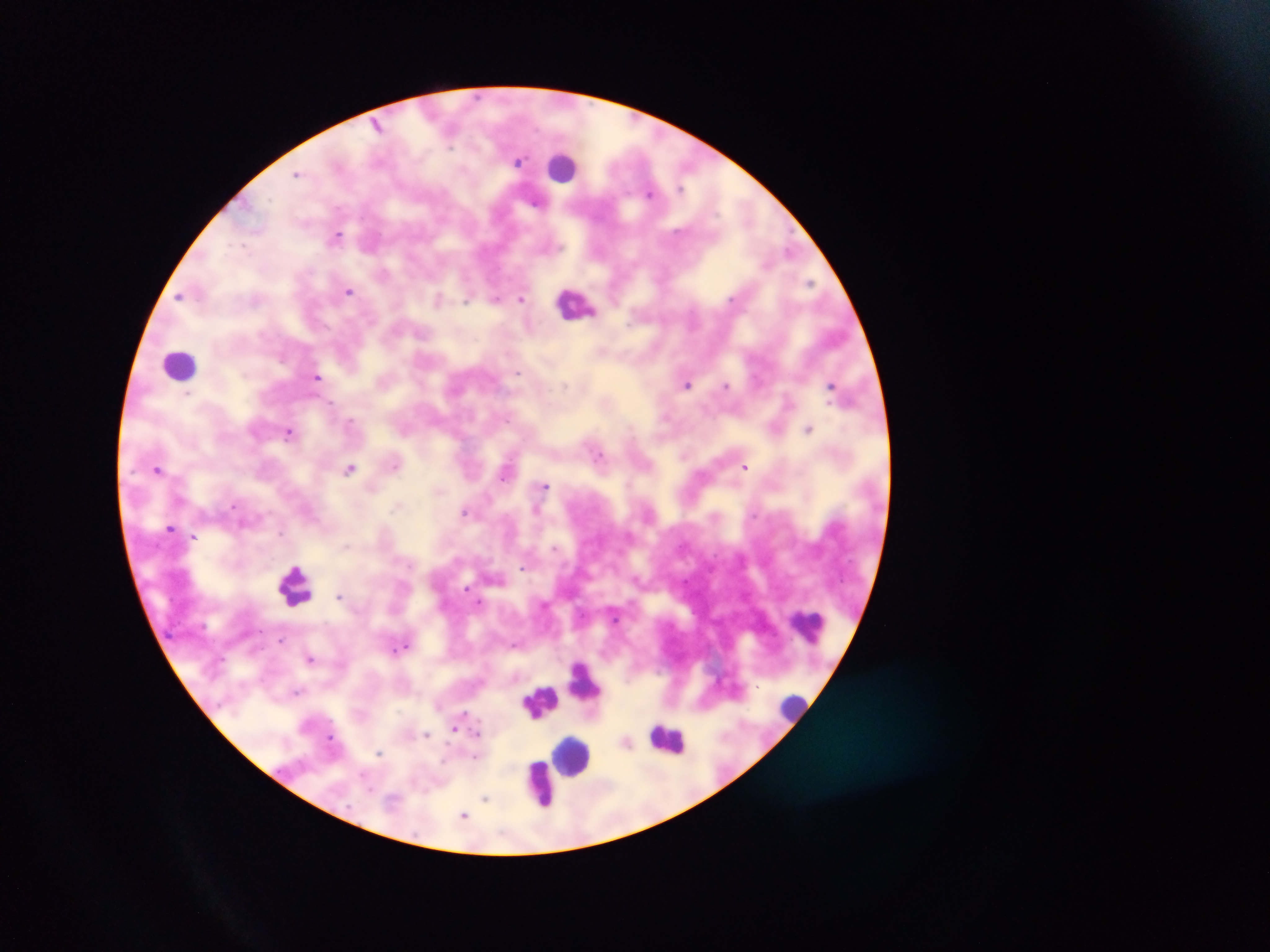

Approximate centers as x y in pixels. Leukocyte locations: 559 167; 574 302; 179 364; 298 590; 808 625; 584 683; 537 696; 789 704; 667 730; 566 753; 537 781. Plasmodium parasite locations: 450 146; 297 176; 679 188; 650 194; 536 200; 335 234; 813 282; 348 290; 178 297; 495 298; 522 298; 467 300; 520 373; 318 377; 334 403; 507 418; 351 420; 290 432; 598 453; 350 468; 747 468; 158 469; 504 478; 543 484; 490 499; 233 504; 537 509; 464 512; 242 524; 170 526; 281 531; 193 536; 347 544; 557 549; 522 567; 294 570; 466 587; 341 594; 481 601; 543 602; 615 618; 281 640; 408 644; 516 644; 311 659; 298 692; 463 712; 455 729; 478 733; 427 735; 331 737; 381 753; 474 757; 365 772; 486 798; 464 815. Thick blood film. Image is 1270×952 pixels. Sample from Ghana. Mobile-phone photograph taken through the microscope. One field of view.